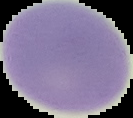
Summary:
  - Result: negative for malaria parasites
  - Preparation: thin blood smear
  - Image type: cell region segmented out of the field of view; surrounding area masked to black
  - Image size: 133×118 pixels